Give the preparation type.
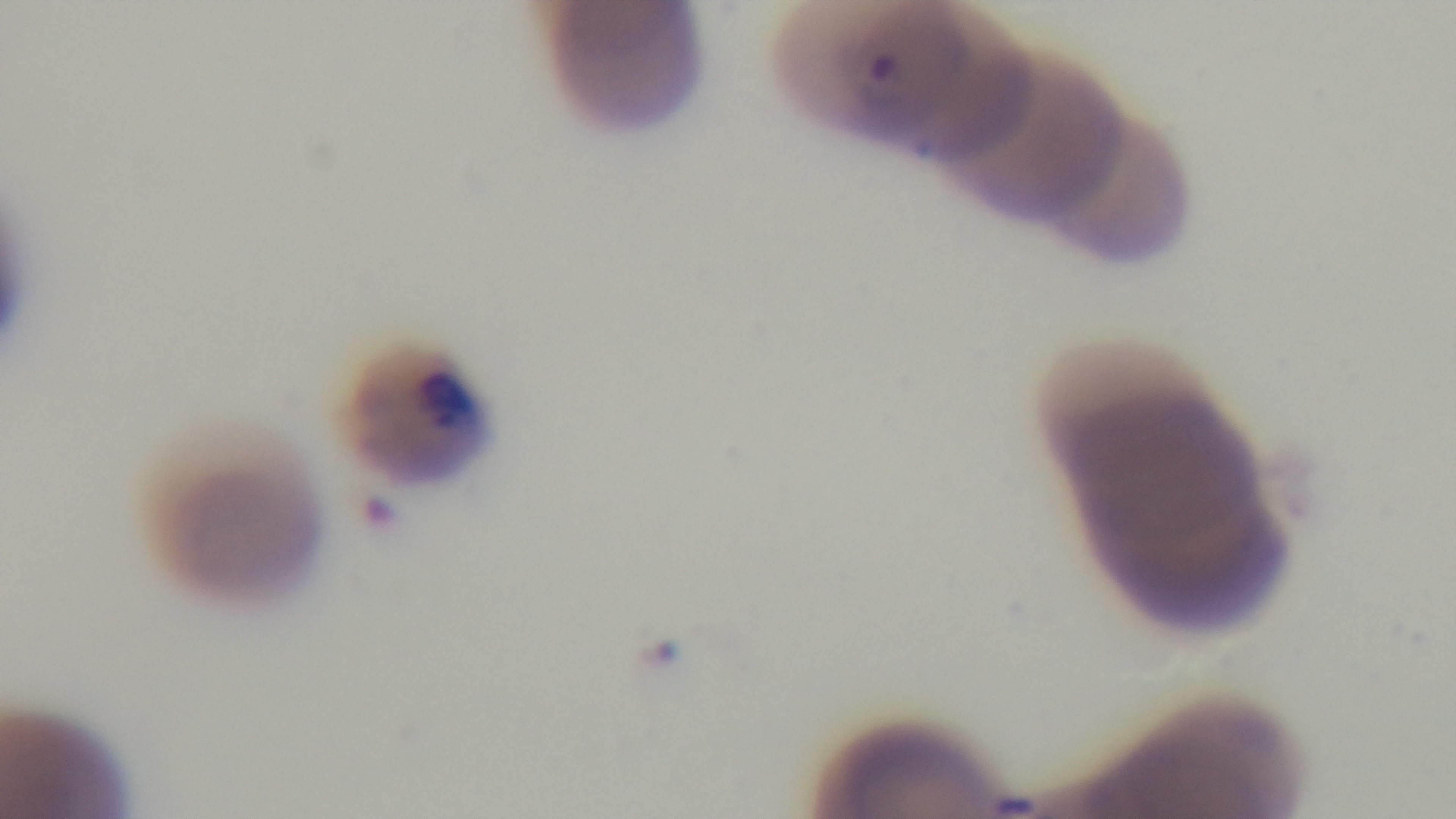
It is a thin blood film.

Mounted 4K digital camera. Giemsa stain. Oil-immersion objective, 100x. Single field of view. Malaria status: infected. Light microscopy.